Give the extent of all uninfected red blood cells.
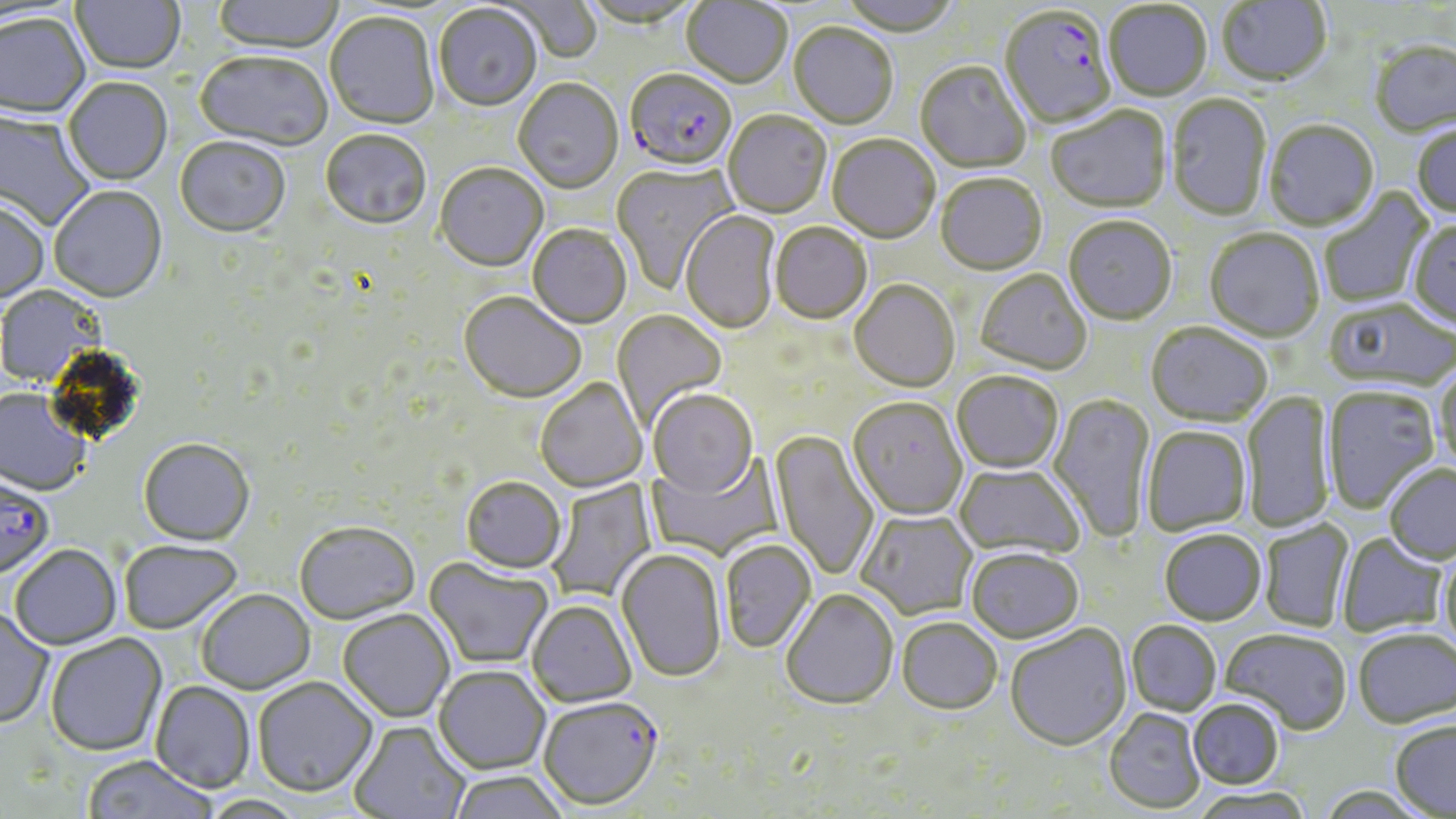

Approximate bounding boxes as [x1, y1, x2, y2] in pixels.
Uninfected red blood cells: [70, 0, 185, 76], [213, 0, 345, 56], [579, 0, 700, 31], [837, 0, 961, 39], [501, 1, 603, 66], [680, 1, 792, 90], [1216, 1, 1332, 90], [1104, 2, 1212, 103], [433, 6, 542, 113], [324, 13, 439, 131], [1, 15, 91, 120], [788, 24, 898, 130], [1370, 42, 1456, 140], [194, 53, 332, 153], [915, 63, 1031, 173], [63, 79, 173, 187], [513, 81, 623, 195], [1167, 95, 1272, 222], [1046, 107, 1172, 215], [0, 109, 94, 231], [722, 113, 832, 219], [1264, 122, 1380, 233], [1412, 124, 1456, 219], [320, 131, 431, 233], [827, 135, 940, 245], [174, 140, 290, 239], [611, 163, 739, 294], [434, 165, 548, 273], [935, 176, 1048, 277], [49, 187, 167, 305], [1319, 187, 1434, 308], [0, 198, 49, 304], [680, 211, 780, 334], [1064, 218, 1176, 327], [1408, 221, 1456, 330], [770, 224, 873, 326], [527, 226, 631, 329], [1204, 230, 1324, 344], [975, 270, 1092, 376], [849, 281, 960, 392], [0, 285, 104, 388], [458, 293, 586, 404], [1324, 300, 1456, 394], [612, 310, 727, 431], [1145, 324, 1273, 427], [1434, 364, 1456, 473], [952, 372, 1063, 474], [535, 379, 647, 493], [1323, 387, 1440, 513], [0, 390, 91, 497], [648, 390, 758, 498], [1242, 390, 1335, 535], [1048, 393, 1156, 544], [847, 398, 968, 520], [1141, 427, 1252, 535], [770, 430, 879, 582], [138, 439, 254, 546], [647, 453, 784, 561], [955, 464, 1084, 560], [1384, 464, 1456, 564], [461, 477, 566, 574], [545, 478, 657, 604], [857, 510, 977, 619], [1260, 520, 1354, 632], [294, 521, 420, 624], [1159, 530, 1266, 626], [1336, 533, 1448, 638], [119, 540, 242, 634], [720, 541, 817, 654], [10, 545, 122, 650], [966, 547, 1084, 644], [616, 549, 727, 684], [1439, 549, 1456, 655], [423, 556, 554, 670], [197, 589, 315, 694], [781, 590, 898, 711], [527, 600, 637, 707], [0, 609, 54, 730], [338, 610, 455, 722], [897, 618, 1003, 715], [1127, 621, 1221, 716], [1005, 624, 1132, 752], [1353, 628, 1456, 728], [1221, 629, 1352, 734], [45, 634, 167, 757], [433, 666, 551, 774], [253, 676, 377, 797], [151, 681, 256, 793], [1188, 699, 1284, 789], [1104, 709, 1205, 813], [1390, 719, 1456, 816], [349, 721, 471, 819], [82, 756, 217, 819], [447, 771, 570, 819], [1190, 787, 1314, 819], [199, 794, 309, 818].

Plasmodium falciparum-infected red blood cell locations: [999, 8, 1117, 131], [624, 71, 737, 175], [0, 480, 53, 579], [538, 697, 664, 811]. Slide-level diagnosis: Plasmodium falciparum. 1000x magnification. Single field of view. May-Grünwald-Giemsa stain. Optical microscopy. Thin blood film. Image is 1456×819 pixels.